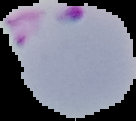

image type = segmented cell region on a black background
image size = 136×121 pixels
malaria status = parasitized
preparation = thin blood film